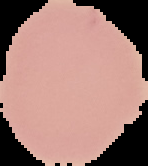
preparation = thin blood smear
image type = cell region segmented out of the field of view; surrounding area masked to black
result = no malaria parasites seen
image size = 148×166 pixels